Identify the blood parasite species.
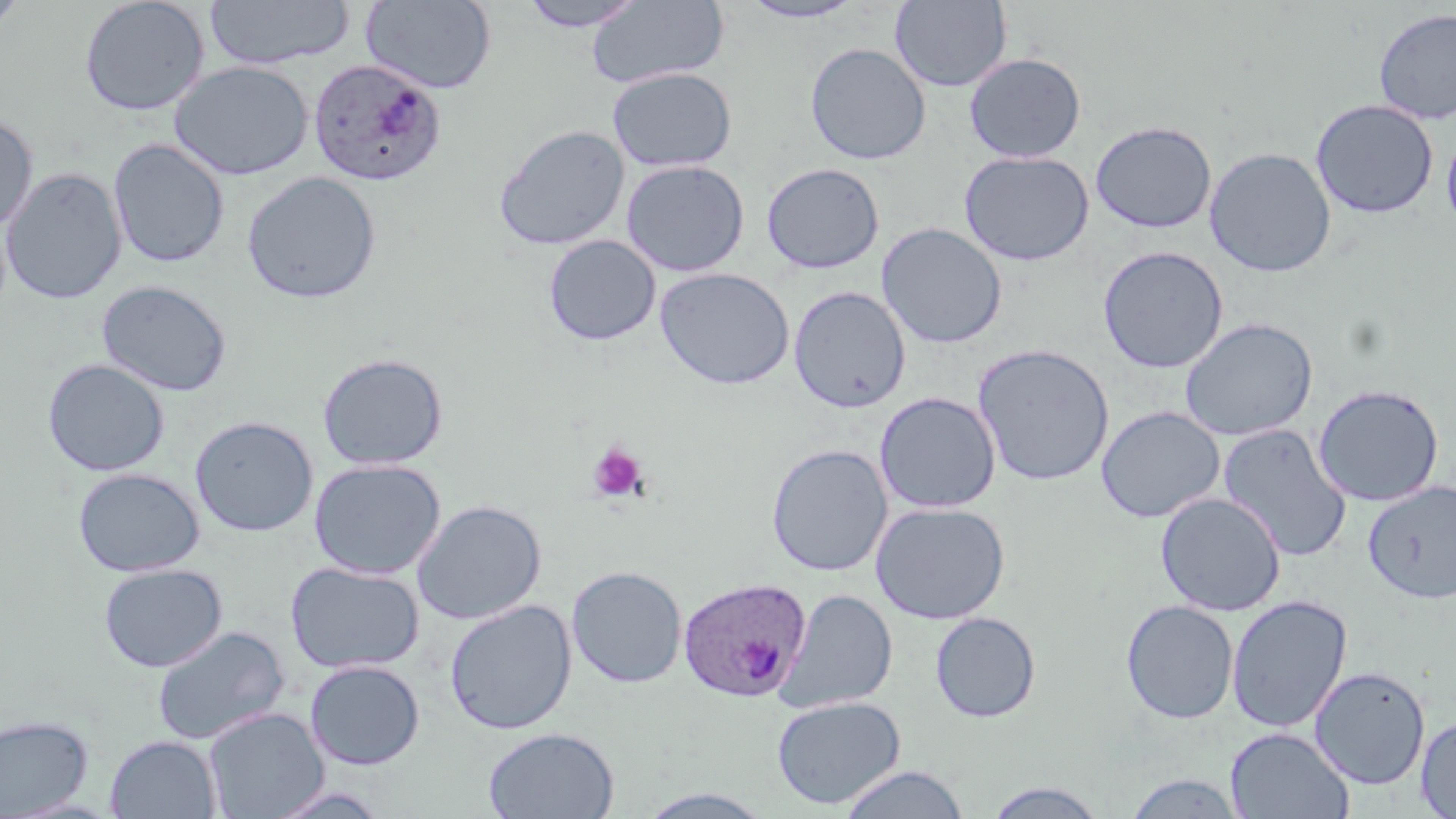
Plasmodium ovale.

Summary:
  - Coordinate format: approximate bounding boxes as named x1/y1/x2/y2 corners in pixels
  - Uninfected red blood cell locations: (x1=79, y1=0, x2=210, y2=117), (x1=204, y1=0, x2=355, y2=70), (x1=362, y1=0, x2=497, y2=94), (x1=587, y1=0, x2=730, y2=89), (x1=890, y1=0, x2=1012, y2=92), (x1=0, y1=1, x2=30, y2=41), (x1=517, y1=1, x2=647, y2=32), (x1=739, y1=1, x2=867, y2=23), (x1=1374, y1=8, x2=1456, y2=125), (x1=805, y1=42, x2=931, y2=165), (x1=964, y1=53, x2=1086, y2=163), (x1=169, y1=61, x2=313, y2=180), (x1=606, y1=67, x2=737, y2=172), (x1=1311, y1=99, x2=1439, y2=219), (x1=0, y1=113, x2=38, y2=233), (x1=1089, y1=120, x2=1217, y2=233), (x1=493, y1=124, x2=630, y2=251), (x1=1442, y1=129, x2=1456, y2=235), (x1=108, y1=138, x2=229, y2=268), (x1=1204, y1=147, x2=1337, y2=277), (x1=959, y1=150, x2=1094, y2=266), (x1=621, y1=160, x2=750, y2=277), (x1=762, y1=163, x2=884, y2=274), (x1=1, y1=168, x2=126, y2=304), (x1=242, y1=171, x2=381, y2=304), (x1=876, y1=223, x2=1007, y2=349), (x1=543, y1=235, x2=661, y2=346), (x1=1097, y1=246, x2=1229, y2=373), (x1=656, y1=268, x2=794, y2=390), (x1=97, y1=280, x2=233, y2=396), (x1=788, y1=286, x2=911, y2=413), (x1=1179, y1=317, x2=1318, y2=441), (x1=973, y1=343, x2=1114, y2=486), (x1=317, y1=353, x2=449, y2=470), (x1=42, y1=359, x2=169, y2=477), (x1=1312, y1=384, x2=1445, y2=507), (x1=875, y1=391, x2=1001, y2=513), (x1=1096, y1=406, x2=1225, y2=523), (x1=190, y1=416, x2=319, y2=536), (x1=1217, y1=424, x2=1352, y2=562), (x1=766, y1=444, x2=892, y2=576), (x1=309, y1=458, x2=446, y2=579), (x1=73, y1=467, x2=204, y2=577), (x1=1363, y1=480, x2=1456, y2=605), (x1=1155, y1=492, x2=1286, y2=616), (x1=411, y1=500, x2=547, y2=625), (x1=871, y1=501, x2=1009, y2=624), (x1=286, y1=561, x2=424, y2=674), (x1=99, y1=563, x2=227, y2=672), (x1=566, y1=565, x2=687, y2=688), (x1=776, y1=589, x2=899, y2=713), (x1=1226, y1=595, x2=1352, y2=733), (x1=444, y1=599, x2=577, y2=735), (x1=1120, y1=599, x2=1239, y2=724), (x1=930, y1=611, x2=1041, y2=723), (x1=151, y1=625, x2=290, y2=745), (x1=305, y1=659, x2=425, y2=770), (x1=1309, y1=666, x2=1431, y2=790), (x1=771, y1=695, x2=905, y2=809), (x1=204, y1=707, x2=328, y2=819), (x1=0, y1=714, x2=94, y2=817), (x1=1416, y1=716, x2=1456, y2=818), (x1=483, y1=727, x2=619, y2=819), (x1=1225, y1=727, x2=1354, y2=818), (x1=105, y1=735, x2=221, y2=819), (x1=837, y1=765, x2=971, y2=819), (x1=1122, y1=772, x2=1248, y2=818), (x1=981, y1=780, x2=1111, y2=817), (x1=639, y1=789, x2=773, y2=819)
  - Platelet locations: (x1=588, y1=442, x2=648, y2=502)
  - Plasmodium ovale-infected red blood cell locations: (x1=309, y1=59, x2=446, y2=187), (x1=677, y1=576, x2=811, y2=703)
  - Preparation: thin blood smear
  - Magnification: 1000x
  - Stain: May-Grünwald-Giemsa
  - Modality: optical microscopy
  - Image size: 1456×819 pixels
  - Field of view: single